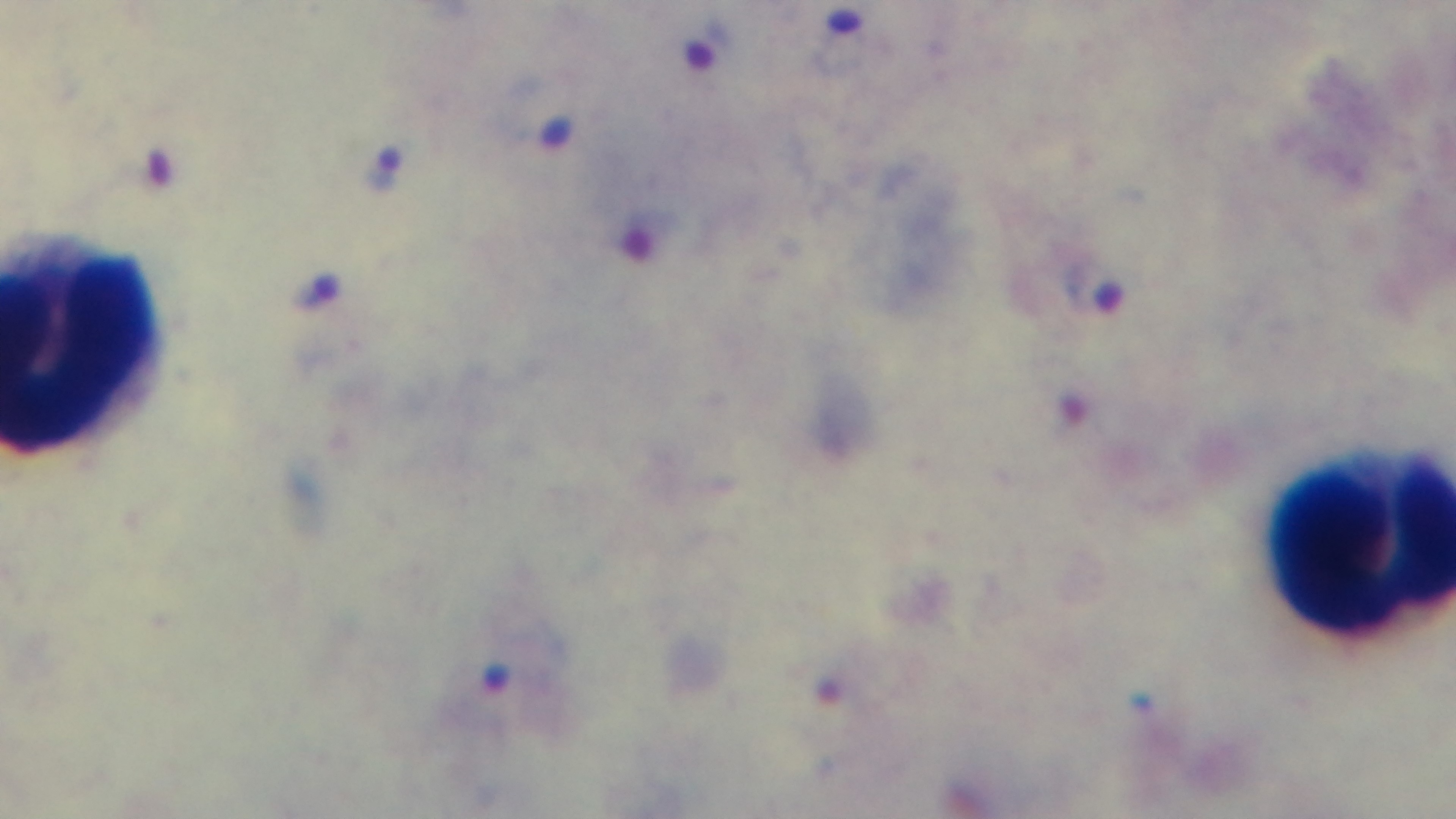

{
  "objective": "100x oil immersion",
  "stain": "Giemsa",
  "capture": "mounted 4K digital camera",
  "preparation": "thick smear",
  "malaria_status": "infected",
  "modality": "light microscopy",
  "field_of_view": "one from the slide"
}